Classify this cell by malaria status.
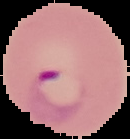
It is parasitized.

Image is 130×139 pixels. Segmented cell region on a black background. From a thin blood smear.